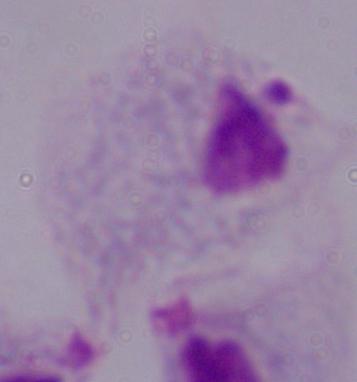

Photomicrograph. A trichomonad is shown. Captured at 1000x magnification.